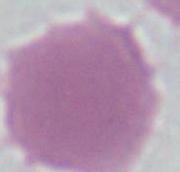

Summary:
  - Magnification: 1000x
  - Modality: photomicrograph
  - Identification: erythrocyte